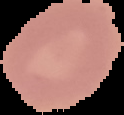

result: no malaria parasites detected
preparation: thin blood smear
image_type: segmented cell region on a black background
image_size: 124×115 pixels